Classify this cell by malaria status.
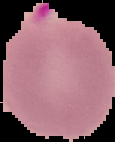
It is parasitized.

Summary:
  - Image type: cell region segmented out of the field of view; surrounding area masked to black
  - Image size: 115×142 pixels
  - Preparation: thin blood film